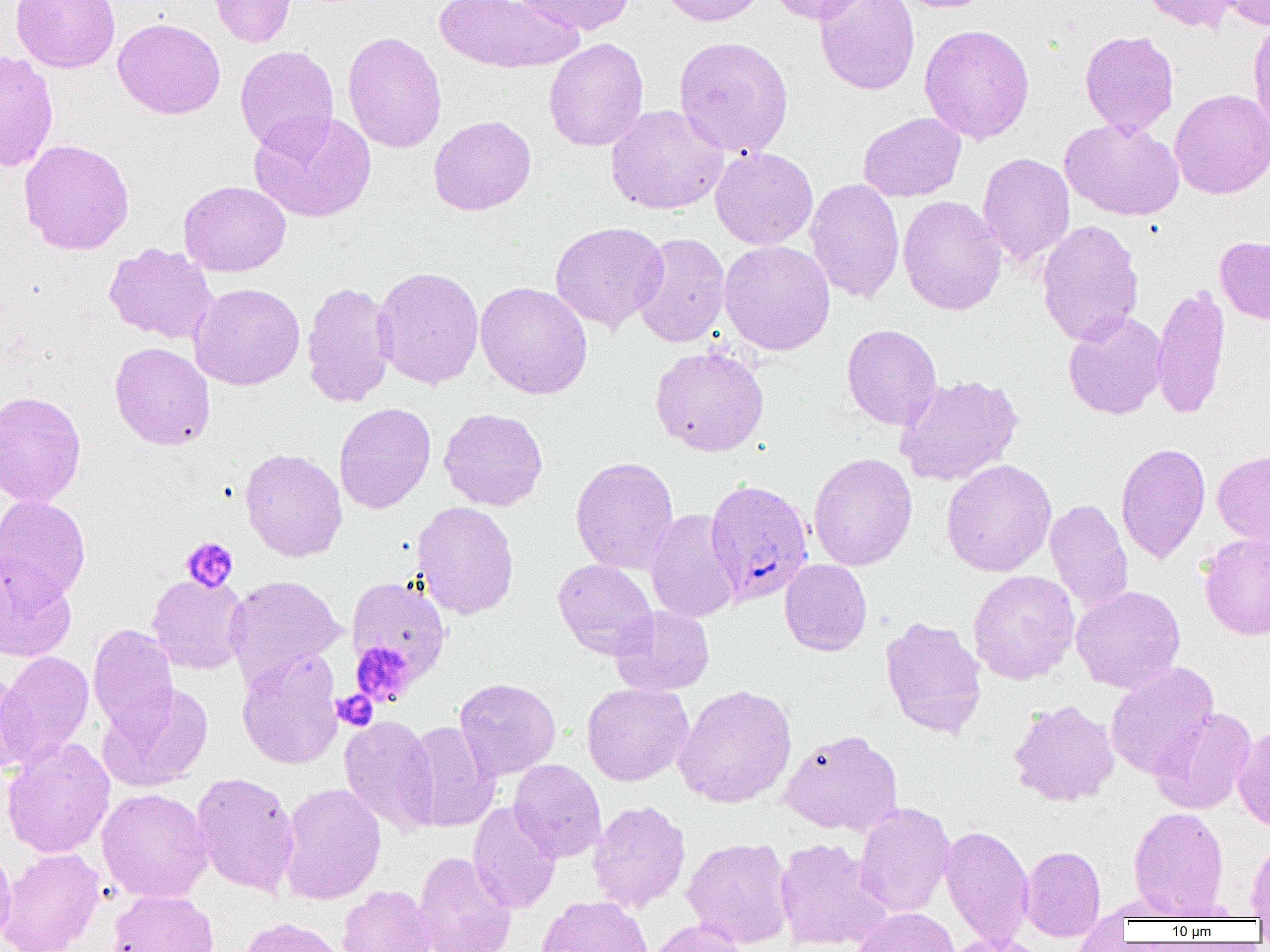
{
  "plasmodium_falciparum_infected_red_blood_cell_locations": "approximate bounding boxes as named x1/y1/x2/y2 corners in pixels: (x1=705, y1=478, x2=814, y2=606)",
  "slide_level_diagnosis": "Plasmodium falciparum",
  "platelet_locations": "approximate bounding boxes as named x1/y1/x2/y2 corners in pixels: (x1=180, y1=536, x2=238, y2=592), (x1=350, y1=641, x2=417, y2=707), (x1=331, y1=689, x2=378, y2=732)",
  "uninfected_red_blood_cell_locations": "approximate bounding boxes as named x1/y1/x2/y2 corners in pixels: (x1=11, y1=0, x2=121, y2=72), (x1=207, y1=0, x2=298, y2=47), (x1=434, y1=0, x2=580, y2=74), (x1=511, y1=0, x2=636, y2=36), (x1=658, y1=0, x2=768, y2=26), (x1=764, y1=0, x2=874, y2=24), (x1=814, y1=0, x2=920, y2=95), (x1=891, y1=0, x2=997, y2=13), (x1=1142, y1=0, x2=1241, y2=33), (x1=1220, y1=0, x2=1270, y2=29), (x1=113, y1=17, x2=226, y2=120), (x1=1248, y1=19, x2=1270, y2=136), (x1=918, y1=23, x2=1035, y2=144), (x1=1080, y1=30, x2=1180, y2=136), (x1=342, y1=31, x2=447, y2=153), (x1=673, y1=36, x2=794, y2=158), (x1=543, y1=38, x2=648, y2=152), (x1=234, y1=45, x2=339, y2=155), (x1=0, y1=52, x2=59, y2=172), (x1=1169, y1=89, x2=1270, y2=199), (x1=605, y1=104, x2=728, y2=215), (x1=249, y1=111, x2=376, y2=223), (x1=858, y1=112, x2=966, y2=202), (x1=428, y1=115, x2=537, y2=215), (x1=1060, y1=118, x2=1184, y2=221), (x1=18, y1=138, x2=135, y2=255), (x1=710, y1=147, x2=818, y2=250), (x1=977, y1=152, x2=1075, y2=268), (x1=805, y1=178, x2=905, y2=303), (x1=178, y1=181, x2=291, y2=276), (x1=898, y1=195, x2=1007, y2=315), (x1=1037, y1=219, x2=1144, y2=346), (x1=550, y1=221, x2=669, y2=332), (x1=631, y1=232, x2=731, y2=348), (x1=1215, y1=236, x2=1270, y2=325), (x1=718, y1=240, x2=835, y2=355), (x1=104, y1=242, x2=218, y2=345), (x1=372, y1=266, x2=484, y2=390), (x1=301, y1=281, x2=396, y2=408), (x1=475, y1=281, x2=593, y2=399), (x1=189, y1=282, x2=305, y2=390), (x1=1152, y1=283, x2=1230, y2=420), (x1=1063, y1=310, x2=1168, y2=420), (x1=842, y1=324, x2=942, y2=430), (x1=109, y1=342, x2=215, y2=450), (x1=650, y1=345, x2=769, y2=457), (x1=894, y1=373, x2=1024, y2=486), (x1=0, y1=390, x2=87, y2=507), (x1=334, y1=402, x2=436, y2=513), (x1=439, y1=407, x2=548, y2=511), (x1=1116, y1=442, x2=1210, y2=564), (x1=240, y1=448, x2=347, y2=562), (x1=1212, y1=450, x2=1270, y2=546), (x1=808, y1=452, x2=917, y2=571), (x1=570, y1=456, x2=679, y2=574), (x1=941, y1=459, x2=1056, y2=577), (x1=0, y1=494, x2=91, y2=602), (x1=1045, y1=498, x2=1133, y2=614), (x1=411, y1=501, x2=519, y2=620), (x1=645, y1=509, x2=742, y2=623), (x1=1198, y1=533, x2=1270, y2=640), (x1=0, y1=555, x2=77, y2=662), (x1=552, y1=559, x2=658, y2=659), (x1=780, y1=559, x2=872, y2=656), (x1=968, y1=570, x2=1080, y2=684), (x1=147, y1=574, x2=250, y2=675), (x1=225, y1=575, x2=345, y2=685), (x1=346, y1=576, x2=451, y2=686), (x1=1071, y1=585, x2=1185, y2=692), (x1=610, y1=606, x2=715, y2=696), (x1=879, y1=616, x2=988, y2=739), (x1=88, y1=624, x2=179, y2=738), (x1=237, y1=648, x2=343, y2=770), (x1=1, y1=651, x2=94, y2=768), (x1=1105, y1=662, x2=1218, y2=779), (x1=1, y1=666, x2=35, y2=775), (x1=454, y1=677, x2=561, y2=781), (x1=581, y1=683, x2=693, y2=786), (x1=673, y1=683, x2=797, y2=808), (x1=98, y1=684, x2=214, y2=792), (x1=1009, y1=698, x2=1120, y2=807), (x1=1151, y1=707, x2=1256, y2=814), (x1=339, y1=714, x2=440, y2=837), (x1=401, y1=720, x2=499, y2=832), (x1=1232, y1=722, x2=1270, y2=831), (x1=780, y1=729, x2=903, y2=836), (x1=1, y1=736, x2=116, y2=858), (x1=508, y1=759, x2=606, y2=862), (x1=191, y1=771, x2=300, y2=896), (x1=279, y1=782, x2=386, y2=905), (x1=96, y1=787, x2=213, y2=903), (x1=588, y1=800, x2=691, y2=912), (x1=467, y1=801, x2=561, y2=914), (x1=854, y1=802, x2=955, y2=917), (x1=1129, y1=806, x2=1229, y2=917), (x1=940, y1=825, x2=1034, y2=945), (x1=682, y1=837, x2=795, y2=947), (x1=773, y1=837, x2=892, y2=950), (x1=1246, y1=837, x2=1270, y2=919), (x1=0, y1=843, x2=17, y2=950), (x1=1020, y1=845, x2=1106, y2=940), (x1=0, y1=847, x2=105, y2=952), (x1=414, y1=850, x2=516, y2=952), (x1=337, y1=884, x2=436, y2=952), (x1=108, y1=889, x2=219, y2=952), (x1=537, y1=896, x2=653, y2=952), (x1=853, y1=907, x2=960, y2=952), (x1=237, y1=917, x2=347, y2=952), (x1=647, y1=920, x2=749, y2=952), (x1=943, y1=934, x2=1052, y2=952)",
  "modality": "light microscopy",
  "preparation": "thin blood smear",
  "image_size": "1270×952 pixels",
  "field_of_view": "one of a larger specimen",
  "magnification": "1000x"
}